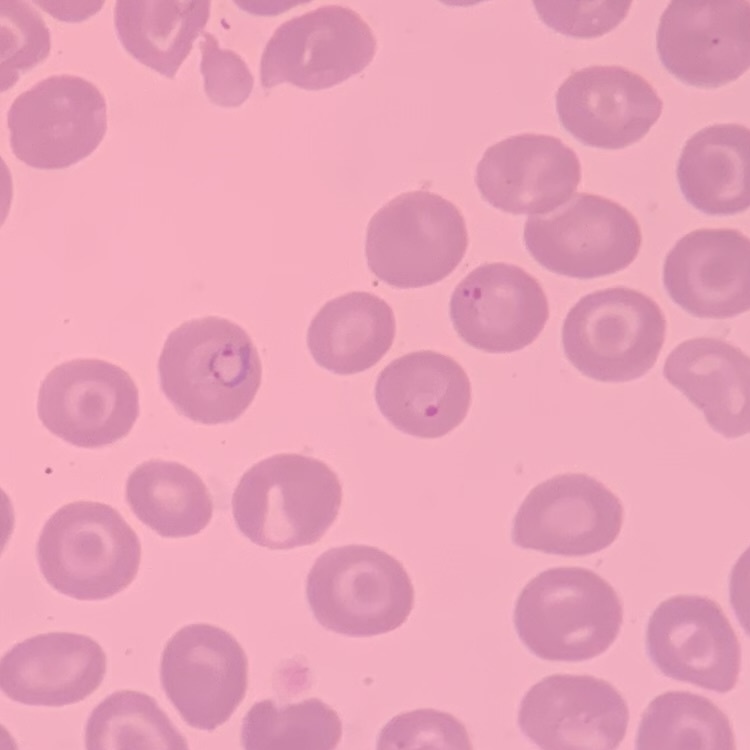
Summary:
  - Red blood cell morphology: no rouleaux formation
  - Image type: square crop of a larger photomicrograph
  - Stain: Field's or Giemsa
  - Preparation: thin peripheral smear